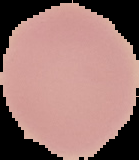
Summary:
  - Image size: 139×160 pixels
  - Preparation: thin blood smear
  - Malaria status: uninfected
  - Image type: segmented cell region with the area outside set to black